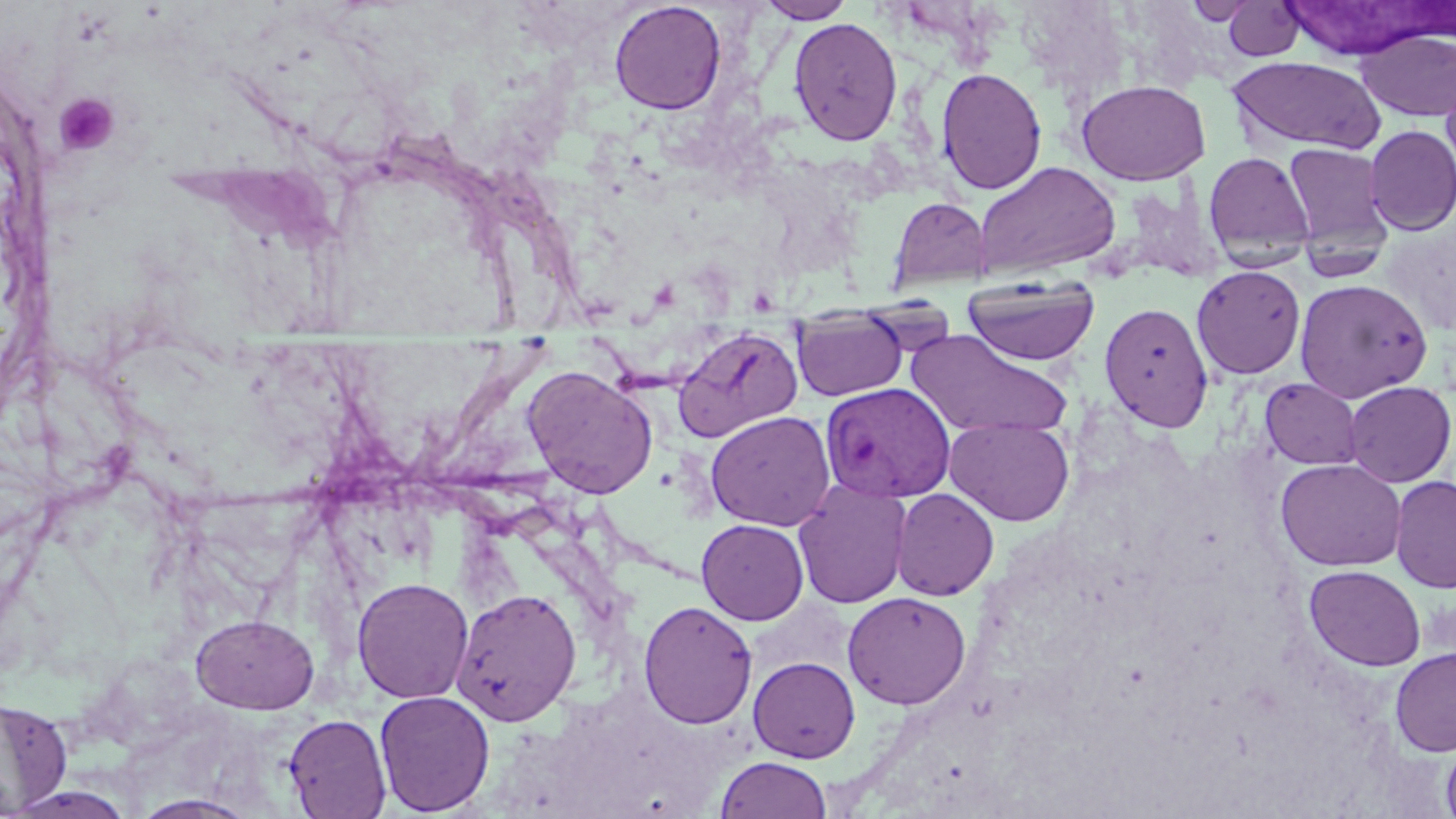 Approximate bounding boxes as named x1/y1/x2/y2 corners in pixels. Plasmodium vivax-infected red blood cell locations: (x1=820, y1=381, x2=955, y2=502). Uninfected red blood cell locations: (x1=609, y1=1, x2=727, y2=115), (x1=756, y1=1, x2=856, y2=23), (x1=1182, y1=1, x2=1262, y2=25), (x1=1223, y1=1, x2=1305, y2=61), (x1=1285, y1=2, x2=1438, y2=59), (x1=788, y1=17, x2=903, y2=146), (x1=1355, y1=29, x2=1456, y2=121), (x1=1227, y1=56, x2=1385, y2=155), (x1=1440, y1=63, x2=1456, y2=185), (x1=936, y1=67, x2=1046, y2=195), (x1=1076, y1=79, x2=1211, y2=185), (x1=1364, y1=126, x2=1456, y2=235), (x1=1283, y1=142, x2=1395, y2=257), (x1=1203, y1=151, x2=1315, y2=265), (x1=973, y1=161, x2=1122, y2=279), (x1=889, y1=197, x2=992, y2=290), (x1=1192, y1=265, x2=1306, y2=379), (x1=963, y1=276, x2=1100, y2=366), (x1=1295, y1=278, x2=1433, y2=403), (x1=1099, y1=301, x2=1214, y2=432), (x1=791, y1=310, x2=908, y2=401), (x1=671, y1=326, x2=802, y2=443), (x1=904, y1=329, x2=1071, y2=441), (x1=522, y1=364, x2=658, y2=498), (x1=1260, y1=378, x2=1362, y2=470), (x1=1343, y1=381, x2=1455, y2=487), (x1=705, y1=410, x2=836, y2=531), (x1=944, y1=417, x2=1075, y2=527), (x1=1274, y1=458, x2=1406, y2=571), (x1=1390, y1=475, x2=1456, y2=594), (x1=793, y1=479, x2=911, y2=609), (x1=892, y1=488, x2=999, y2=600), (x1=697, y1=519, x2=809, y2=625), (x1=1304, y1=565, x2=1425, y2=671), (x1=352, y1=576, x2=474, y2=704), (x1=451, y1=588, x2=582, y2=726), (x1=842, y1=591, x2=971, y2=709), (x1=638, y1=600, x2=758, y2=729), (x1=191, y1=614, x2=319, y2=713), (x1=1390, y1=646, x2=1456, y2=757), (x1=748, y1=656, x2=860, y2=763), (x1=374, y1=690, x2=495, y2=816), (x1=0, y1=698, x2=73, y2=815), (x1=284, y1=714, x2=391, y2=818), (x1=1440, y1=735, x2=1456, y2=819), (x1=714, y1=756, x2=832, y2=817), (x1=130, y1=793, x2=260, y2=818). Platelet locations: (x1=53, y1=92, x2=121, y2=156). Slide-level diagnosis: Plasmodium vivax. Thin blood smear. Optical microscopy. Single field of view. Image is 1456×819 pixels. 1000x magnification. May-Grünwald-Giemsa-stained preparation.